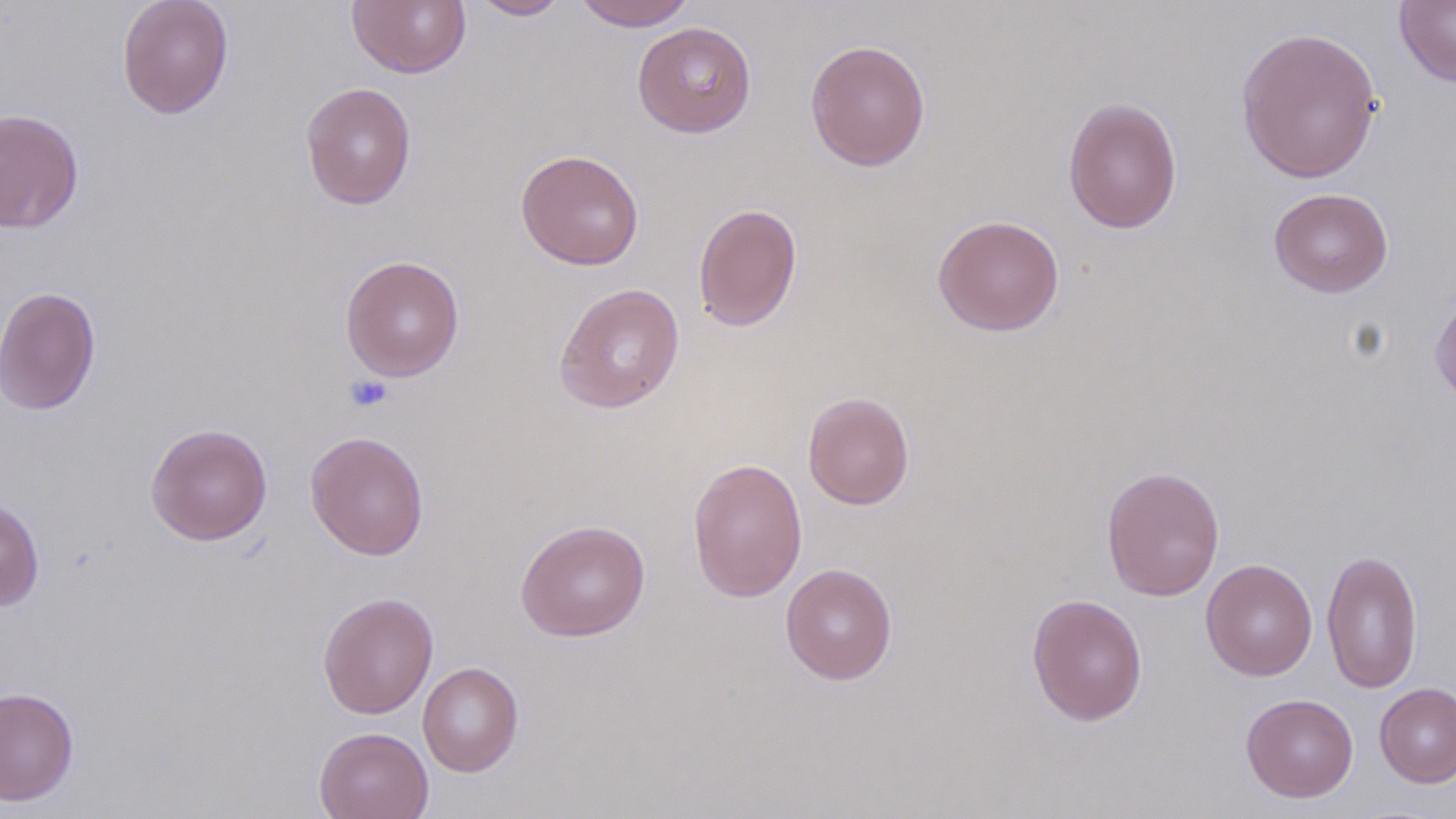
{
  "slide_level_diagnosis": "negative for blood parasites",
  "modality": "optical microscopy",
  "preparation": "thin blood film",
  "platelet_locations": "approximate bounding boxes as (x1,y1)-(x2,y2) corner pairs in pixels: (344,374)-(392,412)",
  "stain": "May-Grünwald-Giemsa",
  "magnification": "1000x",
  "image_size": "1456×819 pixels",
  "field_of_view": "single",
  "uninfected_red_blood_cell_locations": "approximate bounding boxes as (x1,y1)-(x2,y2) corner pairs in pixels: (117,0)-(234,118), (467,0)-(572,20), (573,0)-(697,31), (1395,0)-(1456,89), (346,1)-(471,78), (632,22)-(757,138), (1235,26)-(1383,184), (805,39)-(931,171), (300,81)-(417,210), (1062,96)-(1183,235), (0,107)-(84,234), (515,149)-(645,270), (1268,187)-(1394,297), (693,203)-(803,332), (932,214)-(1065,336), (340,255)-(465,381), (1430,282)-(1456,410), (554,283)-(685,414), (0,285)-(102,416), (802,391)-(914,510), (145,423)-(272,545), (305,431)-(430,560), (687,458)-(808,603), (1100,466)-(1225,601), (0,496)-(45,611), (514,519)-(651,642), (1321,548)-(1423,694), (1201,558)-(1318,681), (780,563)-(897,685), (318,591)-(439,719), (1026,593)-(1148,727), (418,661)-(524,777), (1374,682)-(1456,787), (0,686)-(80,807), (1241,693)-(1358,802), (314,726)-(434,819)"
}